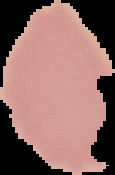

From a thin blood smear. Image is 115×175 pixels. Malaria status: uninfected. Segmented cell region on a black background.